Identify the parasite.
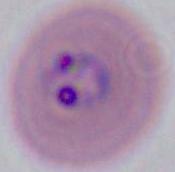
This is Plasmodium.

{
  "magnification": "400x or 1000x",
  "modality": "micrograph"
}